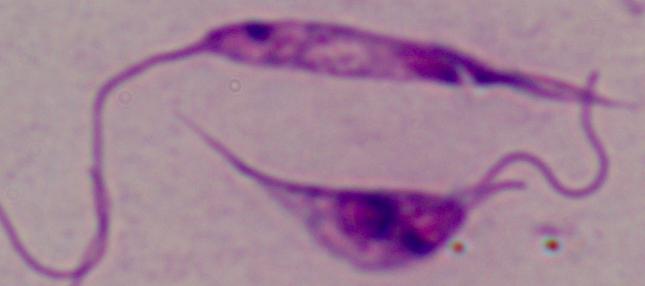

1000x magnification. Photomicrograph. A Leishmania parasite is seen.